Name the cell type shown.
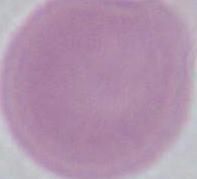
This is an erythrocyte.

magnification: 1000x
modality: photomicrograph